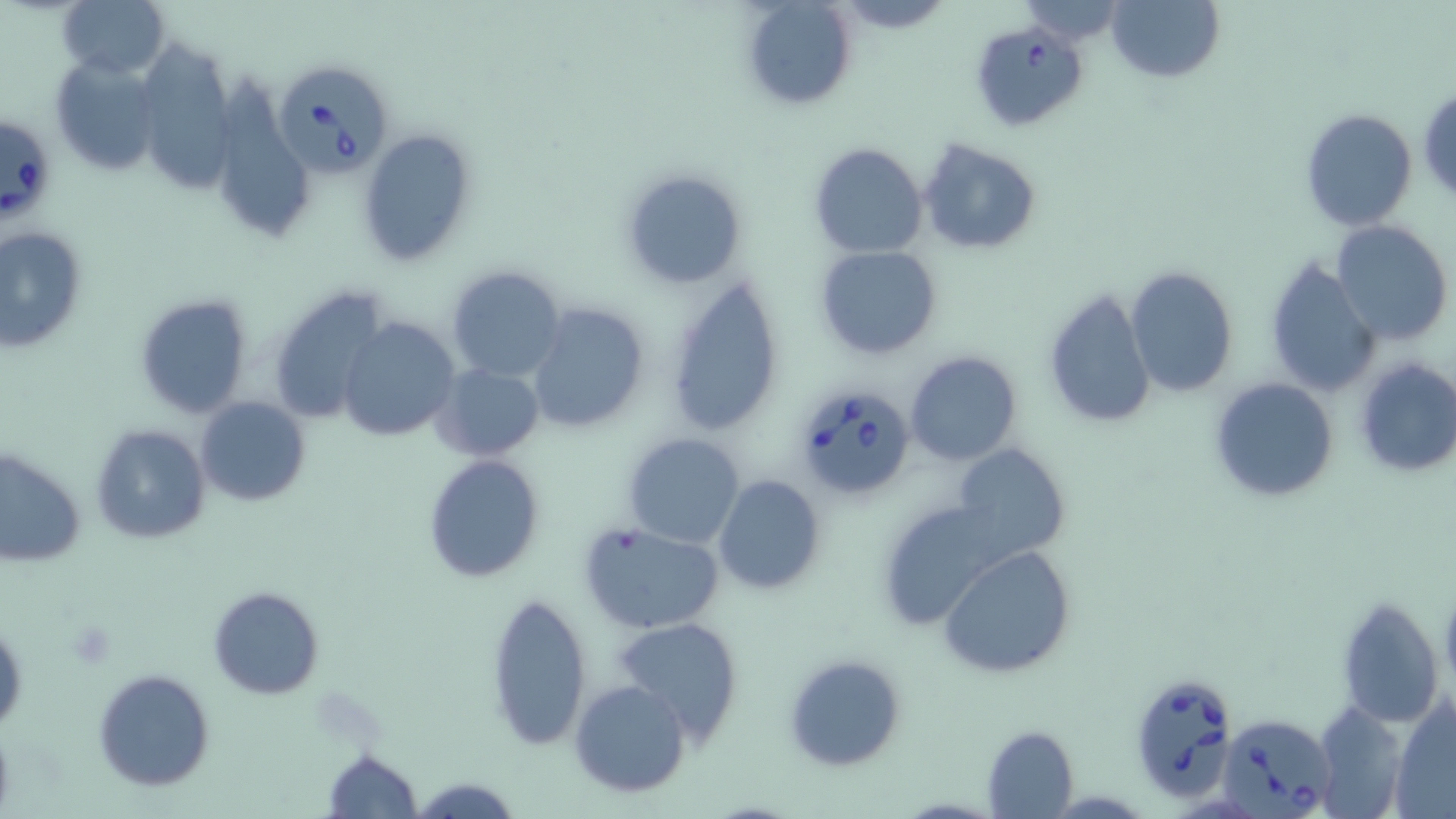

slide-level diagnosis = Babesia divergens
modality = optical microscopy
magnification = 1000x
stain = May-Grünwald-Giemsa
preparation = thin blood film
platelet locations = approximate bounding boxes as (x1, y1, x2, y2) in pixels: (68, 622, 116, 667)
uninfected red blood cell locations = approximate bounding boxes as (x1, y1, x2, y2) in pixels: (56, 0, 170, 81), (737, 0, 858, 111), (1106, 0, 1223, 83), (1010, 1, 1130, 45), (49, 58, 163, 179), (1416, 82, 1456, 203), (1300, 108, 1418, 230), (357, 127, 478, 267), (917, 138, 1042, 254), (808, 142, 928, 257), (620, 166, 748, 292), (1331, 221, 1453, 348), (1, 224, 90, 353), (813, 244, 943, 360), (1264, 254, 1381, 397), (446, 265, 566, 383), (1126, 266, 1240, 398), (662, 270, 786, 439), (265, 285, 396, 426), (1043, 287, 1157, 431), (133, 293, 254, 419), (526, 303, 652, 432), (337, 317, 458, 441), (904, 351, 1023, 465), (1353, 358, 1456, 480), (433, 362, 544, 460), (1207, 376, 1340, 504), (195, 396, 310, 506), (90, 424, 211, 545), (623, 433, 743, 547), (948, 443, 1069, 565), (0, 446, 87, 568), (422, 454, 546, 583), (714, 475, 825, 593), (873, 498, 1017, 630), (577, 521, 726, 635), (941, 547, 1078, 679), (207, 586, 325, 698), (484, 591, 593, 752), (1337, 596, 1446, 728), (0, 613, 27, 735), (612, 615, 745, 742), (781, 651, 907, 770), (93, 668, 214, 791), (570, 678, 691, 799), (1389, 696, 1456, 819), (1314, 699, 1407, 819), (981, 725, 1079, 816), (321, 748, 423, 818), (411, 775, 521, 818)
field of view = single
image size = 1456×819 pixels
Babesia divergens-infected red blood cell locations = approximate bounding boxes as (x1, y1, x2, y2) in pixels: (968, 18, 1088, 130), (273, 58, 396, 178), (0, 115, 48, 228), (792, 382, 917, 501), (1129, 673, 1239, 804), (1212, 705, 1346, 817)